Name the parasite shown.
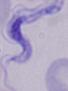
A trypanosome.

Summary:
  - Magnification: 1000x
  - Modality: photomicrograph